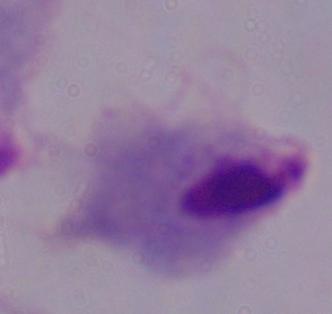

{
  "identification": "trichomonad",
  "magnification": "1000x",
  "modality": "photomicrograph"
}